Classify this cell by malaria status.
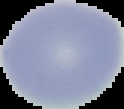
It is uninfected.

Image is 124×109 pixels. Cell region segmented out of the field of view; the surrounding area is masked to black. From a thin blood smear.